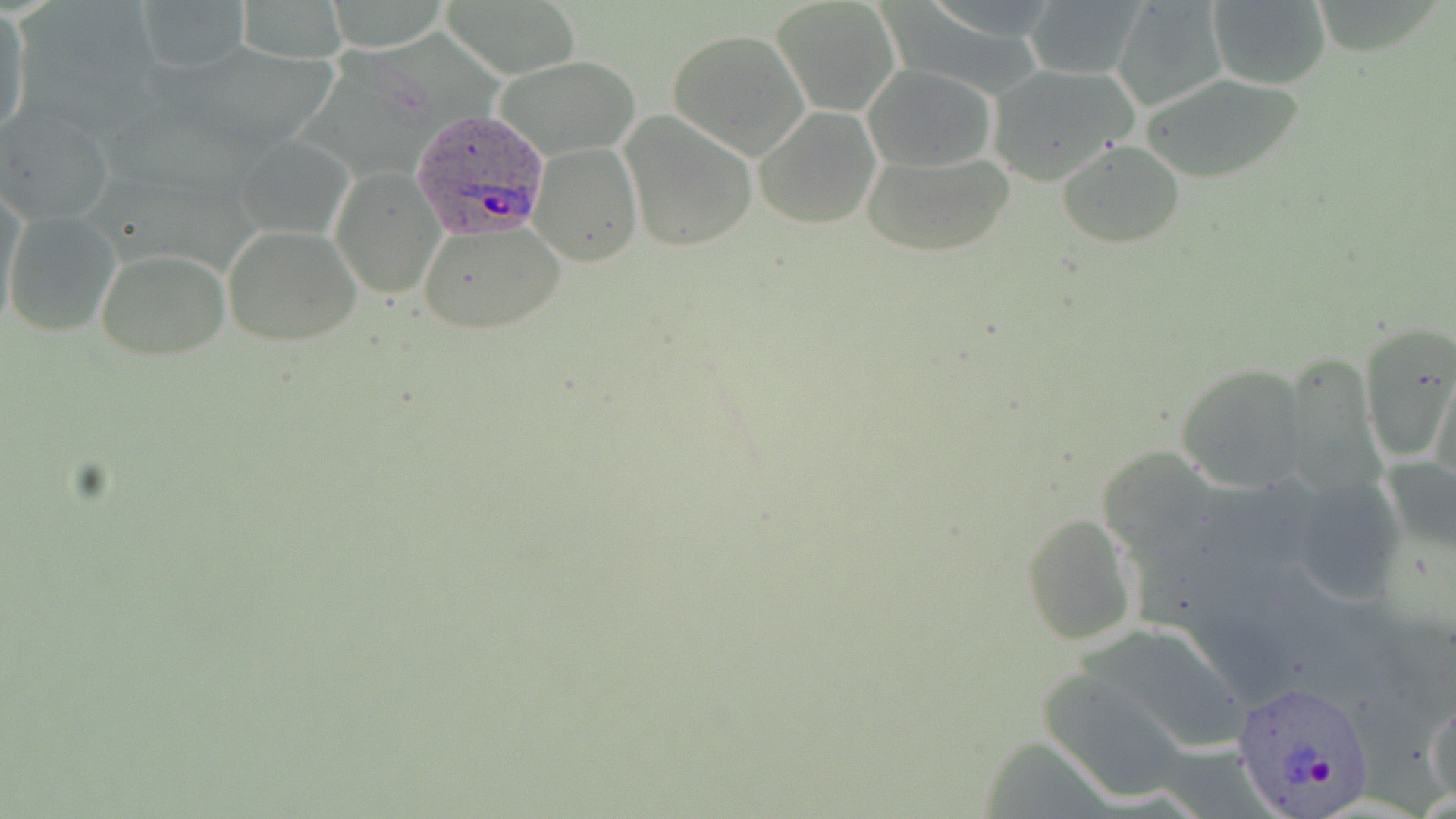
{
  "slide_level_diagnosis": "Plasmodium ovale",
  "preparation": "thin blood film",
  "magnification": "1000x",
  "stain": "May-Grünwald-Giemsa",
  "uninfected_red_blood_cell_locations": "approximate bounding boxes as (x1,y1)-(x2,y2) corner pairs in pixels: (134,0)-(252,76), (323,0)-(453,51), (446,0)-(582,80), (772,0)-(898,115), (1111,0)-(1230,113), (1205,0)-(1331,90), (236,1)-(348,63), (1023,1)-(1147,80), (1,12)-(30,138), (667,27)-(811,158), (497,58)-(638,152), (986,62)-(1138,186), (862,65)-(995,171), (1139,73)-(1308,184), (0,105)-(116,225), (754,106)-(882,228), (618,109)-(757,252), (242,136)-(354,233), (1056,140)-(1186,249), (528,143)-(642,267), (862,148)-(1015,259), (332,168)-(445,299), (1,185)-(27,320), (4,212)-(119,336), (417,219)-(565,334), (224,225)-(361,345), (96,248)-(229,362), (1360,327)-(1456,458), (1176,362)-(1312,490), (1097,445)-(1217,561), (1023,512)-(1142,646), (1036,670)-(1192,802), (1426,687)-(1455,806)",
  "modality": "optical microscopy",
  "image_size": "1456×819 pixels",
  "plasmodium_ovale_infected_red_blood_cell_locations": "approximate bounding boxes as (x1,y1)-(x2,y2) corner pairs in pixels: (409,110)-(552,241), (1234,681)-(1375,815)",
  "field_of_view": "single"
}